Identify the parasite.
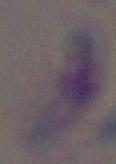

Toxoplasma gondii.

Photomicrograph. Captured at 1000x magnification.